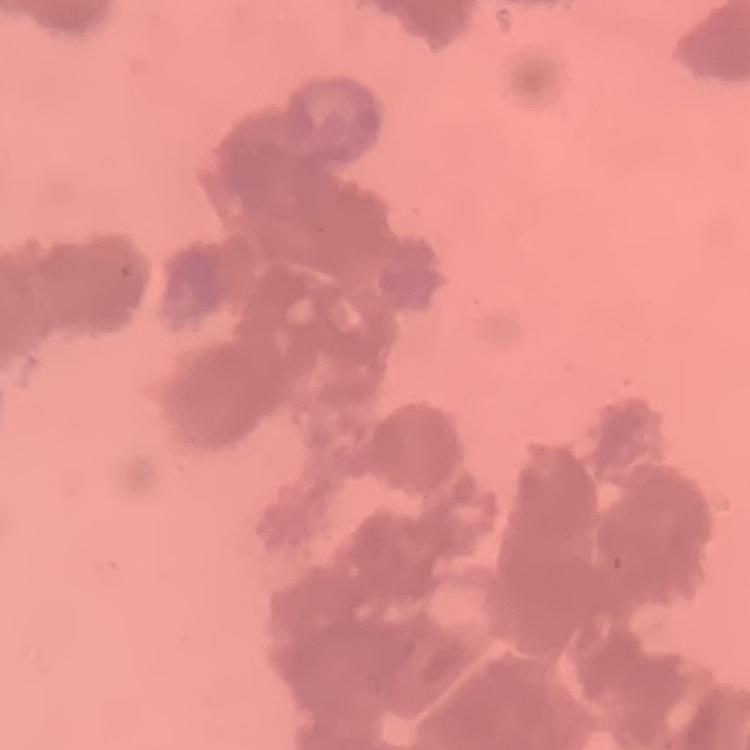 The erythrocytes exhibit rouleaux formation. Field's or Giemsa stain. One tile cut from a larger photomicrograph. Thin peripheral smear.